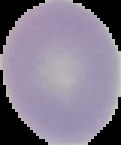
Summary:
  - Malaria status: uninfected
  - Image type: cell region segmented out of the field of view; surrounding area masked to black
  - Image size: 121×145 pixels
  - Preparation: thin blood smear